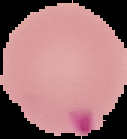
Summary:
  - Image size: 127×139 pixels
  - Malaria status: parasitized
  - Preparation: thin blood smear
  - Image type: cell region segmented out of the field of view; surrounding area masked to black